Report the malaria status of this cell.
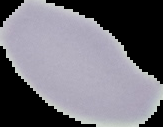

Uninfected.

Summary:
  - Preparation: thin blood film
  - Image type: cell region segmented out of the field of view; surrounding area masked to black
  - Image size: 163×127 pixels